Name the cell type shown.
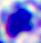
This is a leukocyte.

{
  "magnification": "400x",
  "modality": "photomicrograph"
}